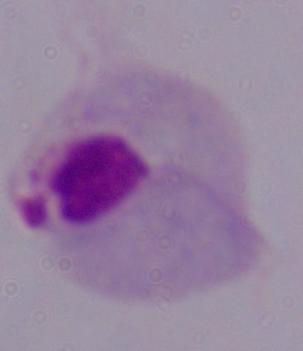
1000x magnification. Photomicrograph. A trichomonad is seen.